Describe the morphology of the red blood cells.
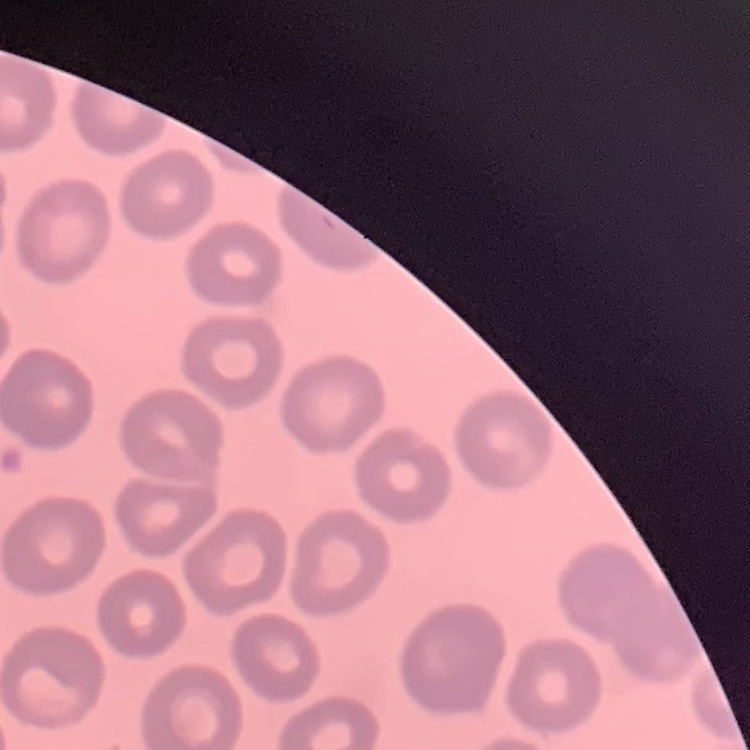
They show no rouleaux formation.

image type = square crop of a larger photomicrograph
stain = Field's or Giemsa
preparation = thin blood film